Comment on the morphology of the red blood cells.
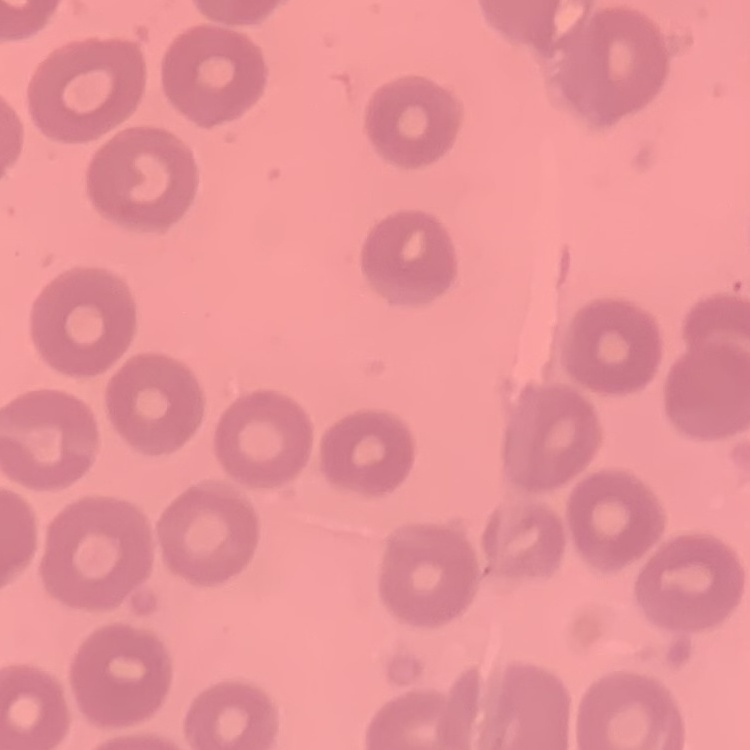

No rouleaux formation.

Square crop of a larger photomicrograph. Thin blood film. Stained with either Field's or Giemsa.